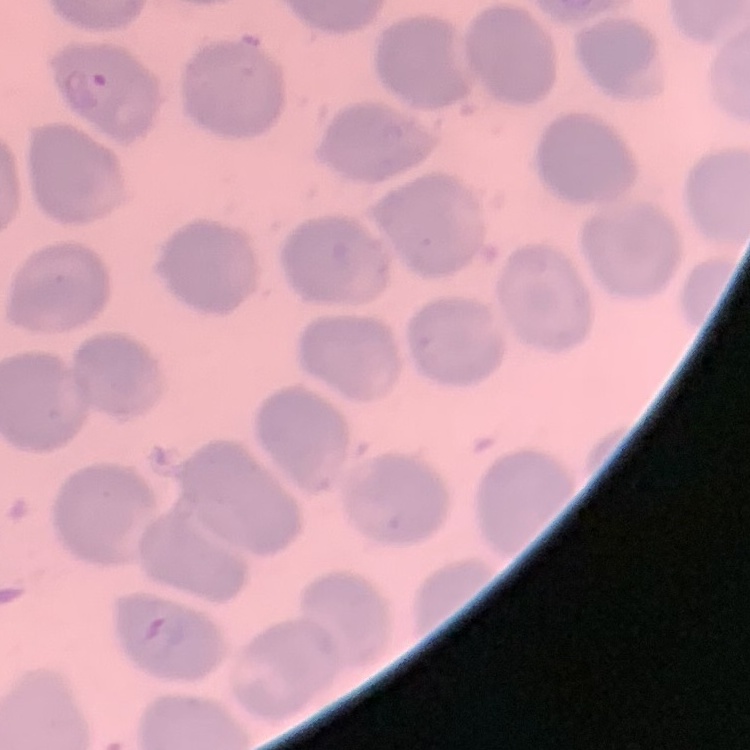
The red blood cells show no rouleaux formation. Field's or Giemsa stain. One tile cut from a larger photomicrograph. Thin blood smear.